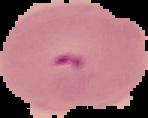

{
  "image_type": "segmented cell region on a black background",
  "preparation": "thin blood smear",
  "malaria_status": "parasitized",
  "image_size": "148×118 pixels"
}